Point out each leukocyte.
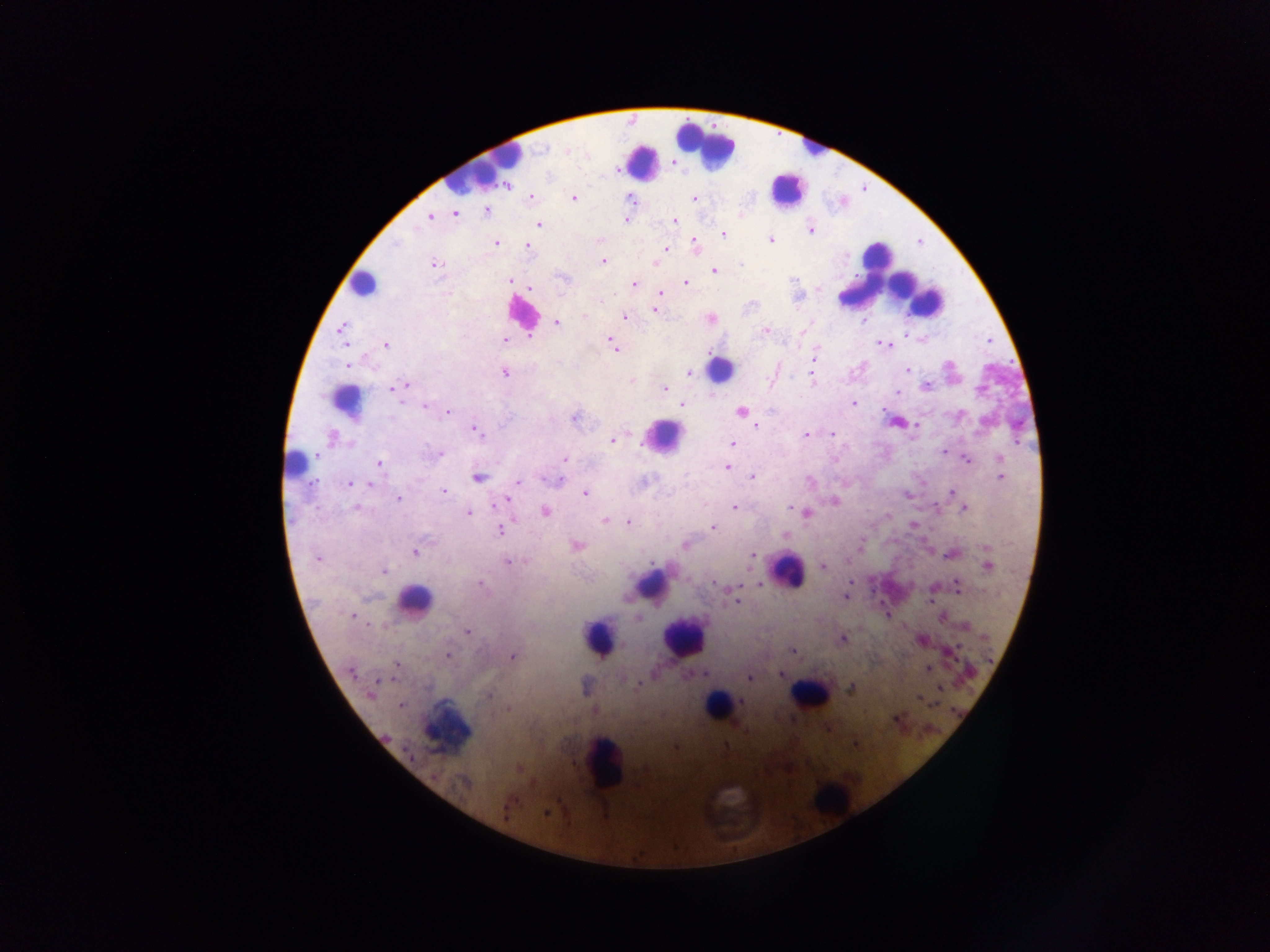

Approximate centers as x y in pixels.
Leukocytes: 705 143; 808 144; 644 161; 480 167; 786 189; 879 267; 887 276; 896 280; 362 283; 521 309; 719 369; 344 401; 665 436; 297 467; 787 569; 651 585; 414 600; 684 636; 599 638; 809 694; 717 706; 444 729; 604 765; 830 798.

Plasmodium parasite locations: 567 151; 507 186; 531 197; 573 198; 694 198; 630 199; 487 211; 455 214; 429 216; 626 220; 674 221; 539 224; 810 230; 723 234; 771 239; 599 240; 694 242; 496 243; 396 244; 527 245; 666 249; 604 261; 655 262; 740 263; 433 264; 714 271; 564 277; 510 280; 686 283; 633 284; 529 289; 660 294; 752 305; 654 311; 584 316; 624 317; 711 319; 557 323; 341 328; 765 330; 528 336; 504 339; 610 341; 879 343; 386 345; 883 345; 614 346; 812 356; 347 365; 907 370; 689 372; 505 374; 773 376; 810 376; 631 381; 404 386; 925 386; 395 388; 665 389; 898 393; 854 403; 682 405; 424 406; 448 412; 741 412; 958 414; 574 418; 985 422; 917 424; 757 427; 476 430; 806 434; 831 434; 333 438; 613 441; 733 443; 942 451; 315 454; 440 454; 1000 457; 565 459; 967 460; 379 463; 727 467; 752 477; 1000 477; 478 478; 559 481; 810 481; 518 482; 350 483; 370 484; 443 491; 951 493; 585 494; 398 498; 507 500; 834 502; 355 507; 790 507; 734 508; 964 509; 545 512; 807 513; 468 514; 604 522; 629 522; 713 528; 500 530; 785 535; 685 545; 576 546; 987 547; 416 552; 949 554; 752 555; 317 559; 508 562; 823 566; 989 566; 384 571; 481 584; 714 584; 758 584; 740 585; 957 586; 845 597; 931 599; 736 601; 887 615; 351 616; 940 617; 639 618; 467 632; 843 638; 922 640; 792 651; 447 656; 512 656; 398 665; 928 668; 351 673; 779 675; 749 679; 378 680; 637 684; 940 688; 851 689; 370 695; 489 696; 919 698; 400 705; 507 709; 897 719; 676 747; 519 769; 645 769; 465 783; 546 813. Image is 1270×952 pixels. Mobile-phone photograph taken through the microscope. Single field of view. Thick blood film. Sample from Ghana.